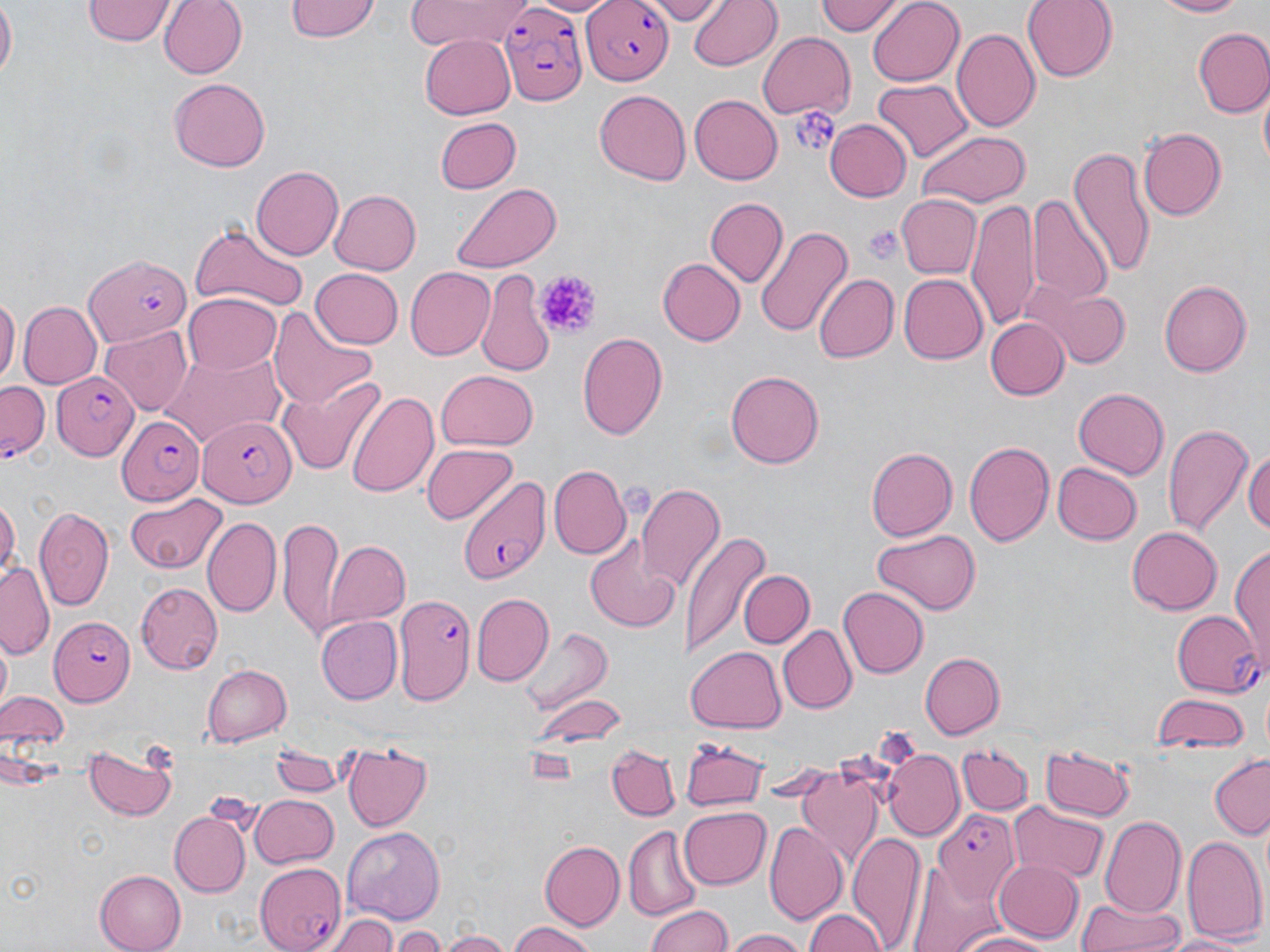

Approximate bounding boxes as (x1, y1, x2, y2) in pixels. Platelet locations: (792, 106, 838, 157), (862, 224, 904, 264), (536, 268, 599, 338). Uninfected red blood cell locations: (0, 0, 16, 87), (157, 0, 247, 80), (287, 0, 378, 43), (402, 0, 534, 50), (533, 0, 615, 15), (646, 0, 725, 23), (688, 0, 783, 71), (817, 0, 899, 38), (866, 0, 963, 88), (1023, 0, 1117, 81), (1149, 0, 1249, 18), (84, 1, 175, 45), (951, 27, 1039, 132), (1191, 27, 1270, 116), (420, 32, 515, 117), (757, 33, 856, 117), (168, 78, 270, 171), (872, 79, 973, 163), (594, 89, 690, 185), (1258, 89, 1270, 173), (689, 94, 783, 186), (435, 116, 521, 194), (823, 119, 909, 203), (1137, 127, 1226, 220), (918, 131, 1028, 207), (1070, 148, 1155, 277), (250, 165, 343, 260), (451, 182, 563, 272), (327, 189, 421, 276), (1029, 195, 1114, 306), (897, 196, 981, 276), (705, 197, 788, 285), (967, 199, 1041, 329), (866, 220, 907, 265), (190, 223, 308, 316), (755, 224, 853, 342), (658, 258, 744, 345), (405, 267, 495, 361), (311, 268, 404, 346), (813, 273, 898, 363), (900, 273, 987, 364), (477, 274, 556, 379), (1159, 279, 1253, 377), (1023, 285, 1133, 368), (0, 291, 17, 388), (184, 294, 282, 375), (17, 302, 101, 390), (270, 304, 377, 408), (984, 317, 1067, 399), (100, 327, 193, 417), (577, 332, 669, 440), (159, 346, 289, 446), (435, 369, 538, 451), (726, 369, 823, 467), (277, 378, 384, 477), (1073, 386, 1169, 477), (348, 389, 438, 499), (1161, 421, 1252, 537), (963, 439, 1054, 546), (423, 444, 517, 523), (866, 444, 957, 540), (1245, 444, 1270, 538), (1053, 461, 1142, 545), (550, 467, 628, 557), (636, 485, 724, 592), (123, 492, 225, 574), (0, 493, 19, 581), (34, 505, 115, 611), (202, 514, 281, 616), (276, 516, 344, 637), (1126, 525, 1221, 616), (871, 527, 982, 614), (585, 533, 683, 631), (681, 533, 765, 655), (1232, 539, 1270, 674), (327, 542, 412, 626), (0, 563, 53, 657), (737, 570, 812, 649), (135, 583, 223, 673), (837, 587, 927, 678), (473, 593, 554, 685), (314, 616, 401, 704), (780, 624, 857, 713), (520, 626, 610, 715), (687, 645, 786, 732), (918, 652, 1004, 740), (202, 664, 292, 745), (2, 691, 67, 749), (1151, 693, 1250, 751), (530, 695, 627, 749), (680, 737, 766, 811), (958, 741, 1032, 813), (84, 742, 178, 822), (342, 744, 433, 831), (1040, 745, 1134, 821), (609, 747, 679, 820), (269, 748, 345, 798), (883, 751, 963, 837), (1209, 756, 1269, 838), (794, 768, 881, 868), (248, 795, 340, 868), (1010, 802, 1108, 885), (678, 806, 770, 888), (170, 810, 251, 896), (1101, 814, 1189, 917), (764, 820, 846, 924), (343, 825, 442, 918), (624, 827, 703, 920), (848, 831, 926, 947), (1181, 835, 1267, 944), (538, 841, 623, 931), (993, 859, 1084, 944), (95, 868, 187, 952), (1074, 897, 1184, 952), (646, 905, 735, 952), (803, 909, 892, 952), (331, 914, 398, 952), (506, 921, 598, 952), (393, 927, 446, 952), (725, 927, 811, 952), (437, 930, 514, 952), (951, 930, 1056, 952), (1165, 931, 1250, 951). Plasmodium falciparum-infected red blood cell locations: (581, 0, 671, 85), (499, 5, 587, 107), (81, 253, 192, 346), (49, 371, 139, 462), (0, 380, 49, 460), (198, 413, 295, 504), (117, 414, 203, 506), (460, 474, 550, 587), (394, 596, 478, 700), (1171, 609, 1262, 694), (48, 615, 132, 706), (932, 807, 1020, 901), (255, 863, 347, 951). Slide-level diagnosis: Plasmodium falciparum. One field of a larger specimen. 1000x magnification. Thin blood film. Light microscopy. Image is 1270×952 pixels. May-Grünwald-Giemsa-stained preparation.